Report the malaria status of this cell.
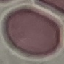

Uninfected.

Summary:
  - Image type: cell patch, automatically extracted from a larger field of view and resized to 64 × 64 pixels
  - Stain: Giemsa
  - Capture: smartphone through the microscope eyepiece
  - Preparation: thin blood smear